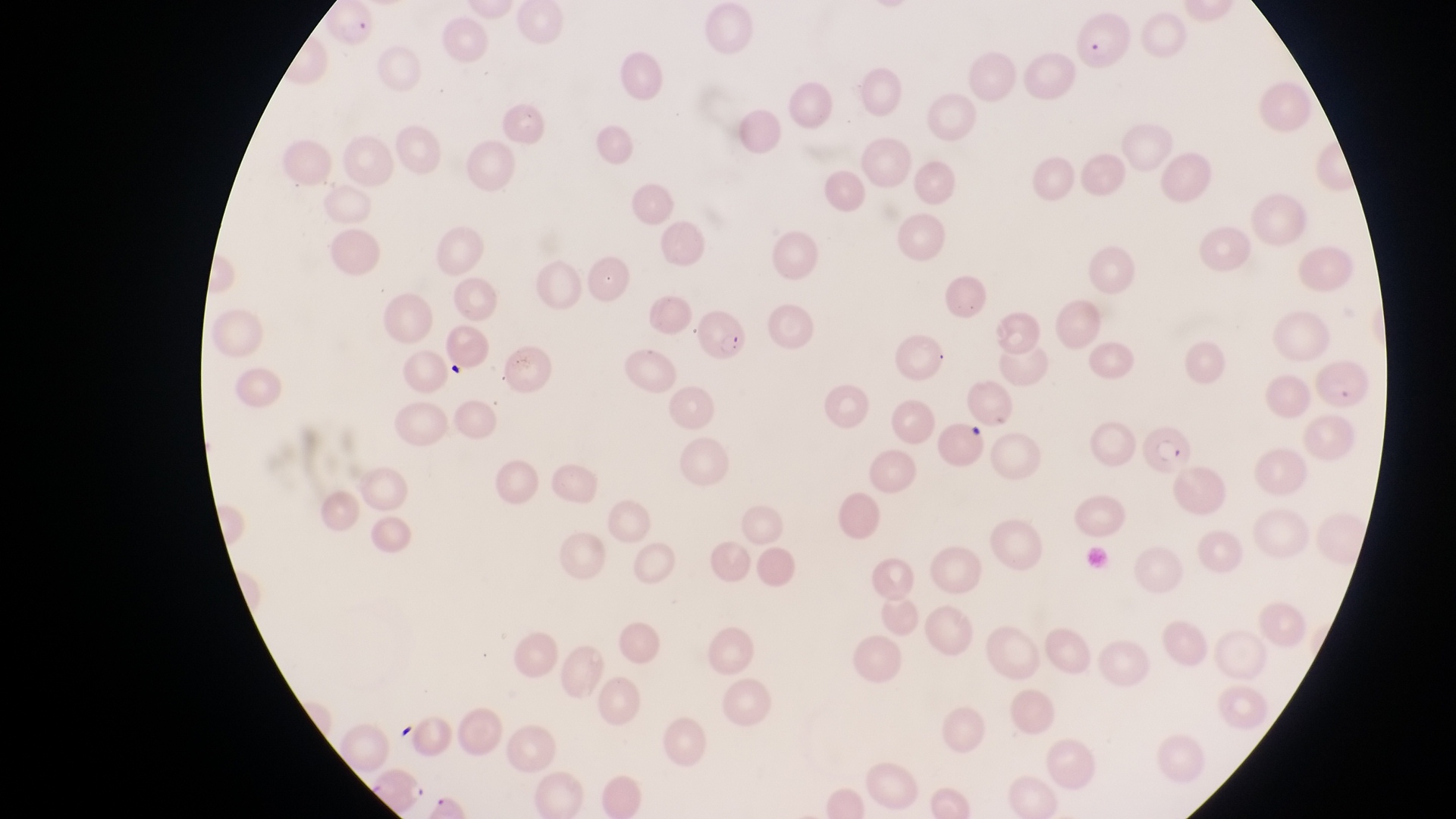

{
  "parasitised_red_blood_cell_locations": "approximate bounding boxes as {left, top, right, bottom} in pixels: {325, 6, 386, 55}, {695, 304, 748, 363}, {1310, 359, 1379, 414}, {1144, 428, 1197, 483}",
  "preparation": "thin blood film",
  "artifact_platelet_like_body_stain_precipitate_or_debris_locations": "approximate bounding boxes as {left, top, right, bottom} in pixels: {1078, 20, 1134, 73}, {962, 425, 995, 448}",
  "magnification": "1000x",
  "capture": "smartphone photograph through the eyepiece of an Olympus CX-23 microscope",
  "image_size": "1456×819 pixels",
  "field_of_view": "single",
  "country": "Uganda"
}